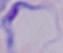
1000x magnification. A trypanosome is seen. Photomicrograph.